Give the position of every malaria parasite and every leukocyte.
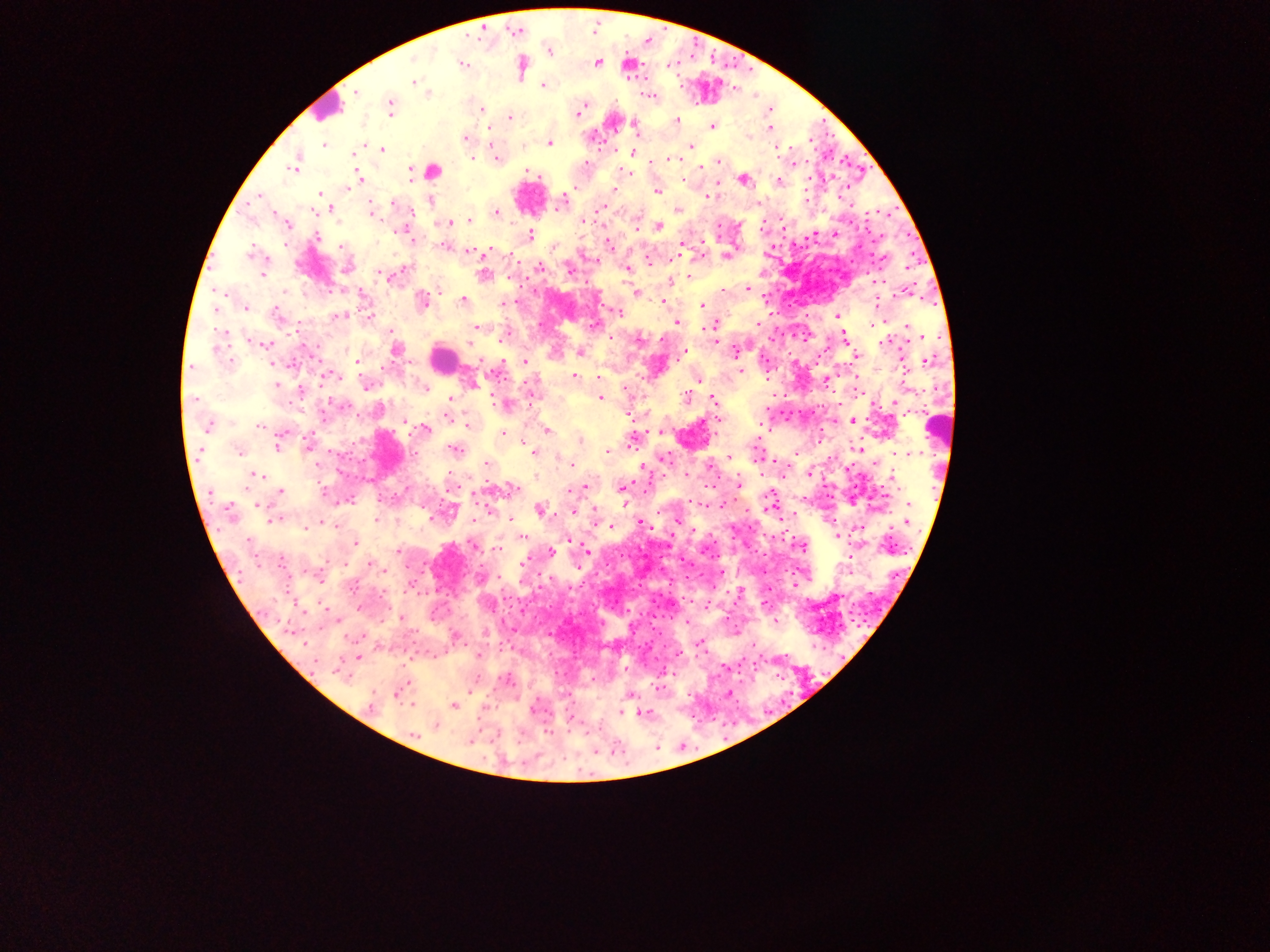
Approximate centers as x y in pixels.
Malaria parasites: 597 62; 463 64; 628 65; 415 83; 542 87; 650 96; 480 108; 391 109; 578 113; 509 116; 677 120; 634 123; 713 126; 768 131; 465 138; 749 138; 550 143; 324 144; 691 147; 383 148; 777 148; 631 151; 495 154; 471 156; 670 159; 721 162; 796 163; 296 166; 293 170; 409 170; 434 170; 528 170; 622 174; 357 175; 741 179; 359 180; 656 191; 710 192; 321 195; 603 206; 370 207; 677 209; 315 212; 496 212; 491 214; 469 219; 585 222; 448 223; 289 225; 657 226; 530 233; 318 236; 609 244; 469 252; 251 253; 481 256; 725 256; 538 267; 569 267; 627 269; 264 275; 381 275; 483 275; 688 277; 669 281; 437 288; 747 288; 904 290; 283 291; 635 291; 221 293; 463 300; 422 301; 662 301; 504 304; 879 304; 702 305; 219 308; 246 308; 618 313; 836 316; 717 321; 676 323; 476 326; 908 328; 223 331; 843 334; 926 336; 886 343; 266 345; 393 352; 579 353; 682 353; 854 356; 926 360; 355 361; 524 361; 901 362; 187 370; 741 370; 332 376; 598 376; 575 378; 697 378; 365 383; 472 384; 276 385; 424 389; 686 397; 598 399; 714 399; 450 400; 895 402; 716 420; 853 422; 404 423; 260 425; 466 425; 208 426; 425 429; 546 431; 277 432; 284 433; 502 433; 580 440; 631 443; 278 447; 237 448; 610 448; 859 449; 456 450; 201 451; 607 451; 533 453; 727 458; 663 460; 486 464; 572 465; 642 467; 809 472; 256 476; 738 478; 740 483; 583 486; 622 489; 280 491; 776 503; 909 503; 257 504; 228 508; 572 510; 542 511; 795 514; 378 517; 275 519; 320 521; 509 521; 639 522; 908 522; 328 523; 315 524; 608 525; 302 526; 337 528; 838 534; 520 537; 567 539; 355 543; 801 545; 474 546; 804 548; 497 549; 397 550; 587 551; 549 552; 368 563; 522 564; 738 591; 837 596; 832 599; 824 602; 325 608; 399 617; 486 633; 454 635; 702 640; 702 644; 304 646; 475 652; 677 654; 360 656; 680 656; 722 669; 664 673; 658 683; 627 696; 411 705; 368 706; 454 706; 621 709; 641 711; 434 726.
Leukocytes: 333 105; 442 354.

image size = 1270×952 pixels
preparation = thick blood film
country = Ghana
field of view = single
capture = mobile-phone photograph through a microscope